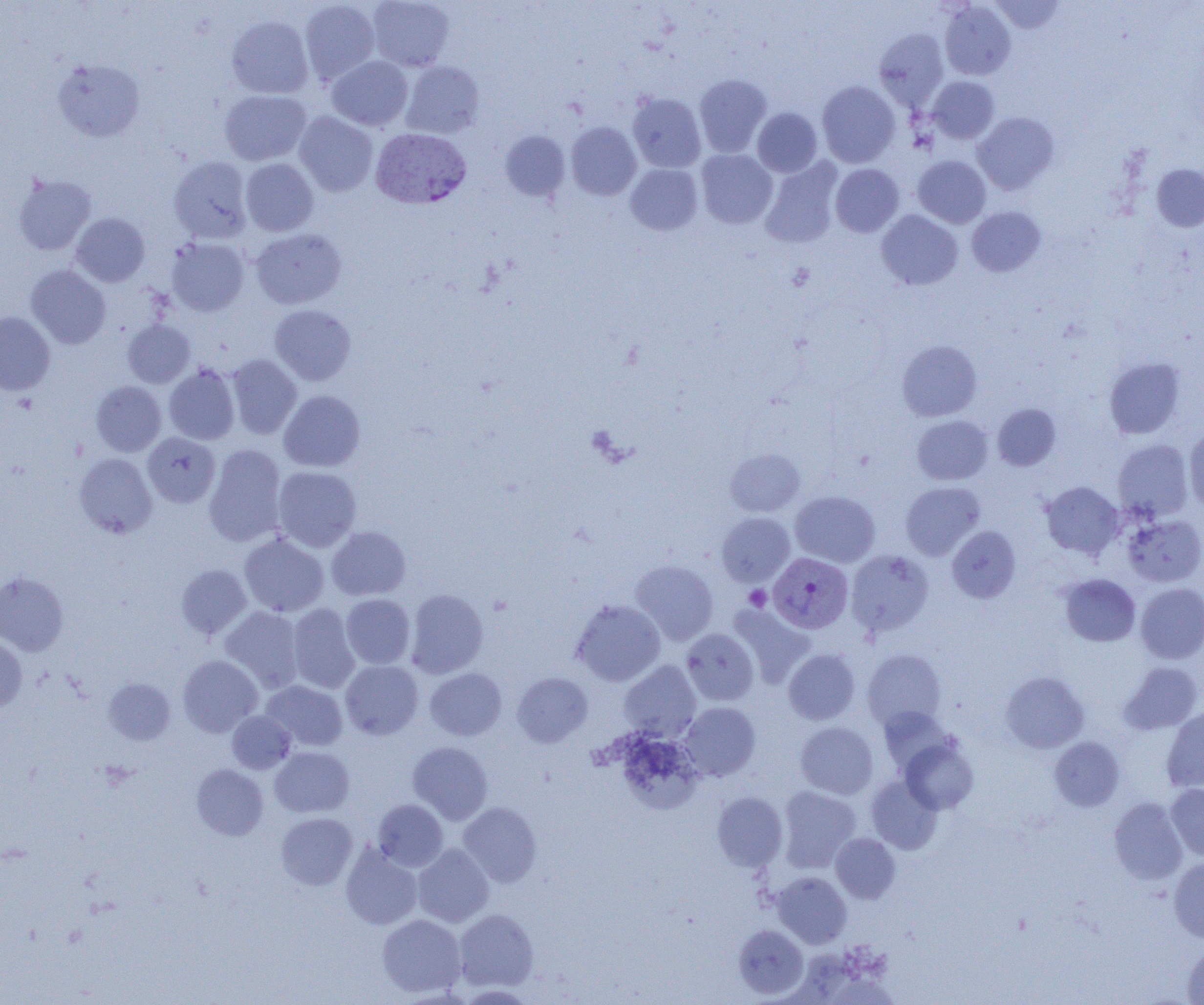
Summary:
  - Coordinate format: approximate bounding boxes as [x1, y1, x2, y2] in pixels
  - Uninfected red blood cell locations: [299, 0, 380, 84], [368, 0, 455, 71], [990, 0, 1065, 34], [939, 1, 1016, 80], [226, 15, 313, 99], [874, 28, 949, 110], [327, 56, 413, 131], [52, 59, 145, 142], [401, 61, 484, 138], [693, 74, 772, 157], [927, 76, 999, 144], [817, 81, 900, 168], [220, 90, 311, 165], [627, 93, 706, 173], [752, 107, 822, 177], [294, 111, 378, 196], [972, 112, 1059, 195], [566, 122, 641, 201], [500, 131, 570, 201], [695, 149, 777, 228], [169, 156, 252, 243], [913, 156, 991, 228], [241, 158, 318, 236], [759, 158, 843, 249], [625, 163, 703, 235], [1152, 163, 1204, 231], [830, 164, 904, 237], [13, 174, 96, 255], [967, 206, 1045, 277], [876, 210, 963, 290], [71, 213, 150, 287], [251, 228, 346, 309], [166, 237, 249, 316], [26, 265, 110, 349], [269, 305, 356, 385], [0, 312, 55, 395], [123, 319, 195, 388], [897, 340, 982, 421], [227, 354, 302, 439], [1104, 357, 1184, 439], [164, 364, 240, 445], [91, 381, 166, 456], [279, 390, 365, 471], [992, 403, 1061, 471], [912, 415, 993, 485], [1184, 426, 1204, 510], [143, 432, 220, 507], [1113, 439, 1193, 521], [204, 444, 287, 546], [725, 448, 805, 516], [74, 453, 157, 538], [273, 466, 362, 552], [1041, 481, 1124, 559], [900, 482, 984, 560], [790, 490, 879, 567], [717, 512, 794, 586], [1123, 514, 1204, 587], [326, 526, 411, 601], [947, 526, 1021, 602], [239, 533, 329, 617], [846, 550, 933, 636], [630, 560, 718, 645], [176, 564, 252, 639], [0, 572, 68, 655], [1061, 574, 1140, 646], [1136, 583, 1204, 663], [405, 589, 488, 678], [341, 594, 415, 669], [571, 599, 665, 686], [287, 604, 360, 694], [728, 604, 813, 686], [220, 607, 304, 692], [681, 628, 759, 705], [0, 638, 27, 712], [783, 649, 860, 725], [862, 649, 947, 730], [178, 655, 262, 737], [340, 660, 423, 739], [619, 661, 701, 741], [1119, 662, 1203, 734], [425, 667, 507, 740], [1001, 671, 1088, 753], [512, 672, 593, 747], [104, 678, 176, 744], [261, 680, 348, 751], [679, 701, 761, 781], [878, 706, 955, 775], [1162, 707, 1204, 792], [227, 710, 296, 773], [795, 721, 878, 799], [612, 730, 703, 814], [900, 737, 979, 813], [1049, 737, 1124, 811], [408, 741, 493, 824], [270, 746, 354, 817], [191, 764, 268, 840], [866, 776, 942, 854], [1166, 783, 1204, 860], [777, 786, 860, 871], [712, 791, 787, 871], [1108, 797, 1188, 884], [373, 799, 448, 871], [457, 801, 542, 886], [276, 812, 357, 890], [830, 833, 901, 903], [340, 842, 423, 929], [413, 843, 494, 927], [1168, 858, 1204, 942], [772, 872, 852, 948], [453, 908, 538, 991], [377, 914, 466, 997], [734, 924, 808, 999], [1183, 942, 1204, 1004]
  - Plasmodium vivax-infected red blood cell locations: [370, 128, 471, 209], [768, 553, 853, 633]
  - Platelet locations: [744, 585, 771, 610]
  - Slide-level diagnosis: Plasmodium vivax
  - Image size: 1204×1005 pixels
  - Field of view: one of a larger specimen
  - Magnification: 1000x
  - Modality: light microscopy
  - Preparation: thin blood smear